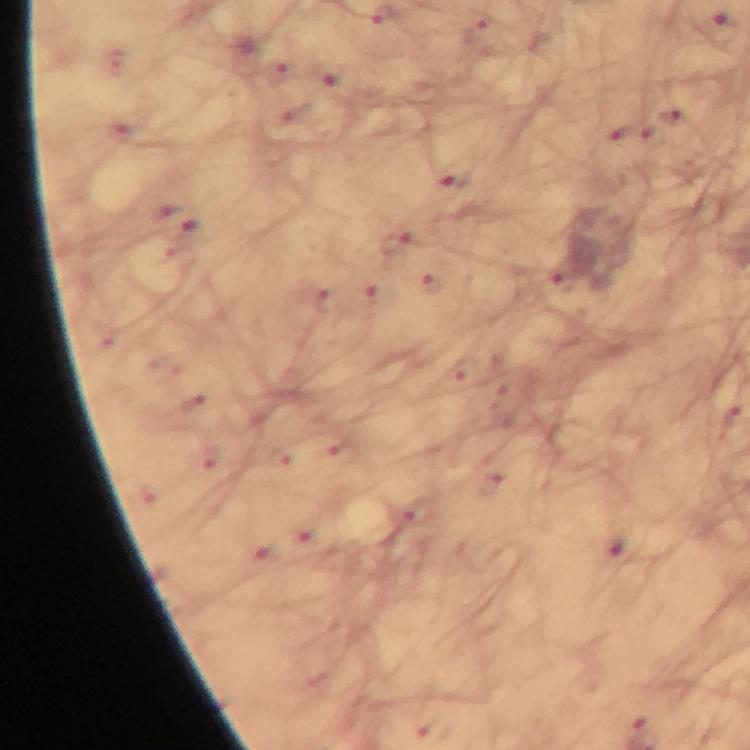 Approximate object centers, in pixels from the top-left corner. Malaria parasite locations: (x=563, y=280), (x=431, y=284), (x=327, y=298). Photographed through the microscope with a smartphone camera. 100x magnification. A crop from one field of view. From a diagnostic examination for malaria. Thick blood smear. Giemsa stain. Image is 750×750 pixels. Immersion oil was used.